Assess the morphology of the erythrocytes.
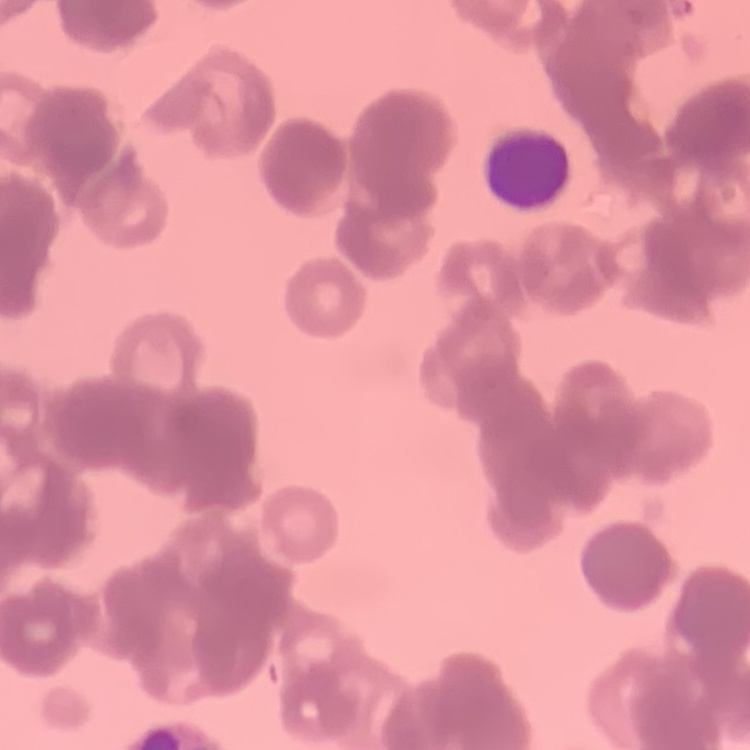

They show rouleaux formation.

{
  "preparation": "thin blood film",
  "stain": "Field's or Giemsa",
  "image_type": "square crop of a larger photomicrograph"
}